State which parasite is depicted.
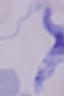

This is a trypanosome.

magnification = 1000x
modality = micrograph